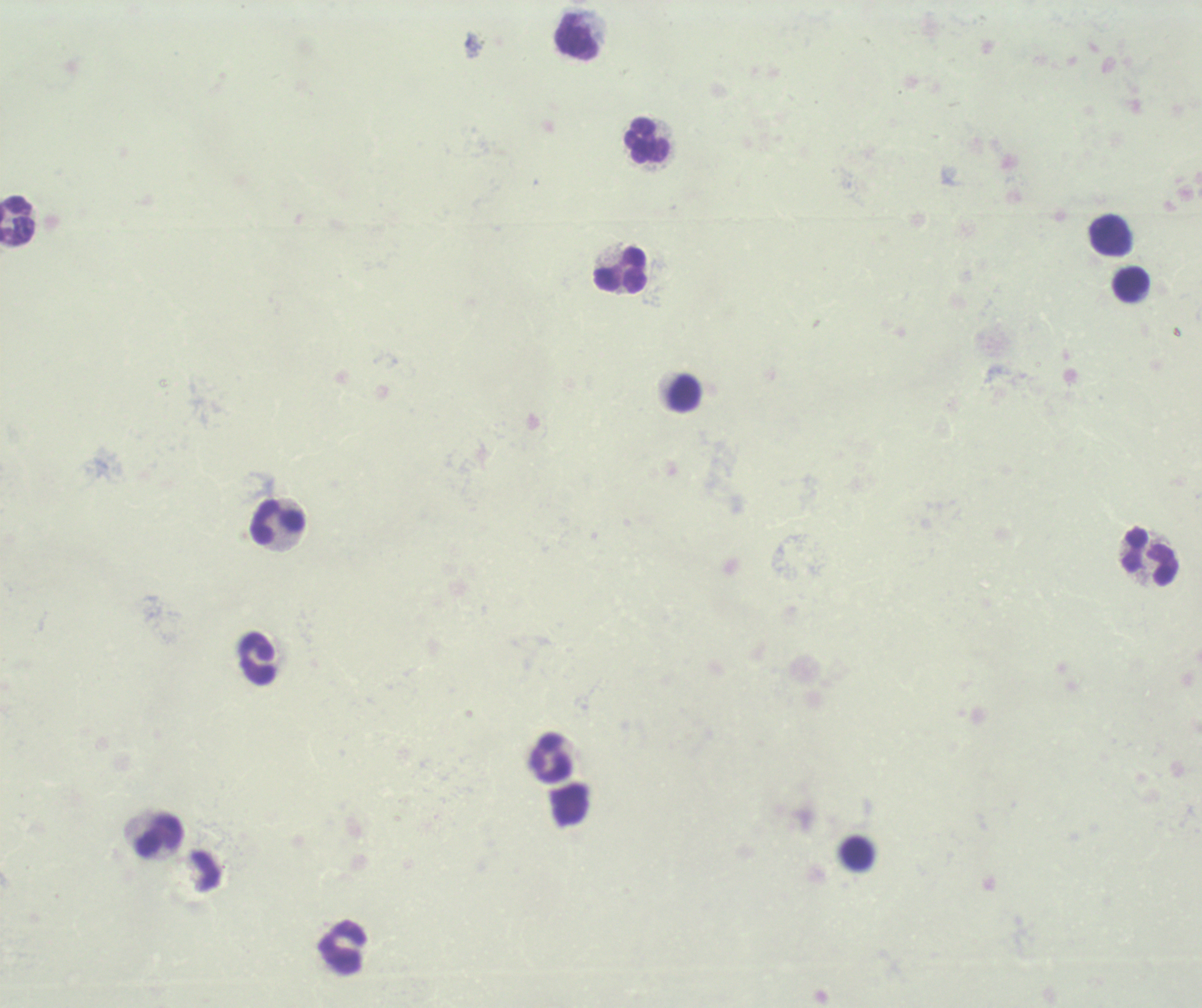 Approximate centers as [x, y] in pixels. Leukocyte locations: [576, 36], [647, 140], [18, 222], [1110, 235], [620, 269], [1131, 285], [684, 394], [278, 522], [1150, 556], [257, 658], [551, 757], [158, 835], [856, 852], [343, 947]. Romanowsky-stained preparation. 100x magnification. Image is 1202×1008 pixels. Thick blood smear. Previously used in a real diagnosis. Background quality: poor. Result: no Plasmodium parasites detected. One field from this slide.